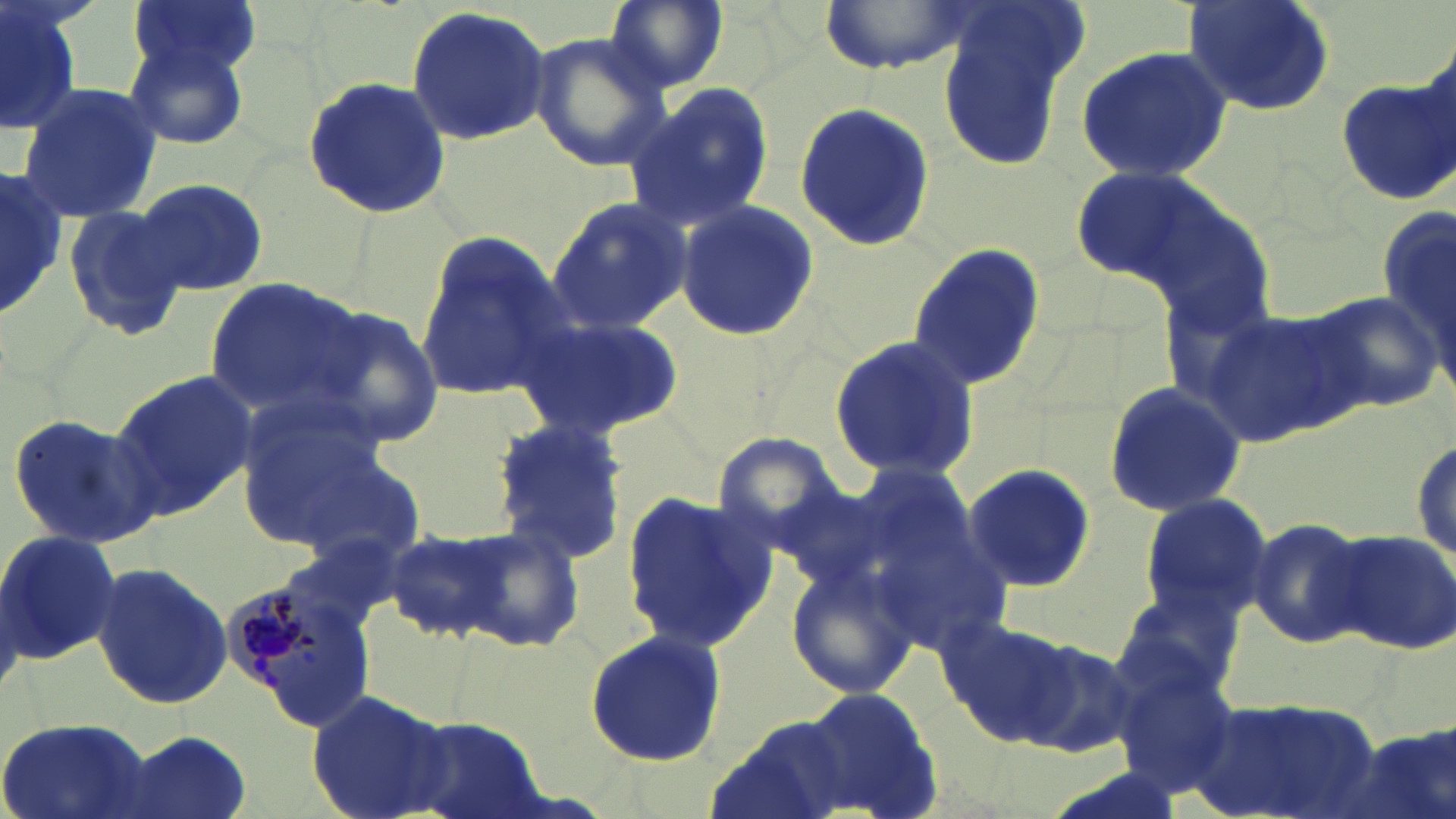 Approximate bounding boxes as [x1, y1, x2, y2] in pixels. Plasmodium malariae-infected red blood cell locations: [220, 569, 379, 730]. Uninfected red blood cell locations: [127, 0, 264, 80], [603, 0, 728, 94], [817, 0, 969, 75], [1180, 0, 1339, 116], [1, 2, 82, 141], [405, 7, 555, 144], [937, 8, 1081, 167], [528, 29, 672, 176], [122, 38, 251, 152], [1073, 46, 1235, 182], [301, 75, 451, 219], [1337, 76, 1456, 206], [624, 80, 775, 229], [16, 84, 162, 222], [793, 101, 935, 255], [1069, 163, 1220, 286], [1, 169, 65, 325], [133, 176, 267, 297], [547, 196, 694, 332], [1379, 197, 1455, 390], [674, 198, 819, 345], [62, 205, 188, 340], [412, 234, 565, 403], [905, 239, 1046, 393], [203, 278, 373, 420], [1306, 291, 1442, 414], [1203, 304, 1367, 447], [307, 305, 447, 448], [515, 310, 684, 440], [829, 333, 980, 482], [107, 370, 261, 521], [1099, 382, 1246, 520], [234, 395, 388, 544], [7, 413, 164, 549], [487, 417, 630, 561], [1410, 433, 1454, 572], [712, 434, 845, 551], [281, 442, 430, 567], [962, 463, 1096, 593], [618, 487, 775, 651], [1136, 491, 1273, 620], [868, 516, 1014, 653], [1245, 516, 1375, 649], [456, 526, 587, 653], [383, 528, 510, 643], [1327, 528, 1456, 654], [0, 530, 120, 666], [87, 560, 232, 713], [785, 560, 920, 702], [1113, 589, 1243, 706], [939, 613, 1072, 740], [580, 626, 732, 768], [1017, 639, 1137, 760], [1113, 662, 1238, 799], [796, 684, 944, 816], [305, 686, 451, 819], [1191, 696, 1389, 819], [401, 715, 549, 819], [0, 716, 157, 819], [703, 716, 853, 819], [1337, 726, 1456, 819], [117, 731, 251, 819]. Slide-level diagnosis: Plasmodium malariae. Image is 1456×819 pixels. Thin blood smear. Single field of view. Light microscopy. Captured at 1000x magnification. May-Grünwald-Giemsa stain.